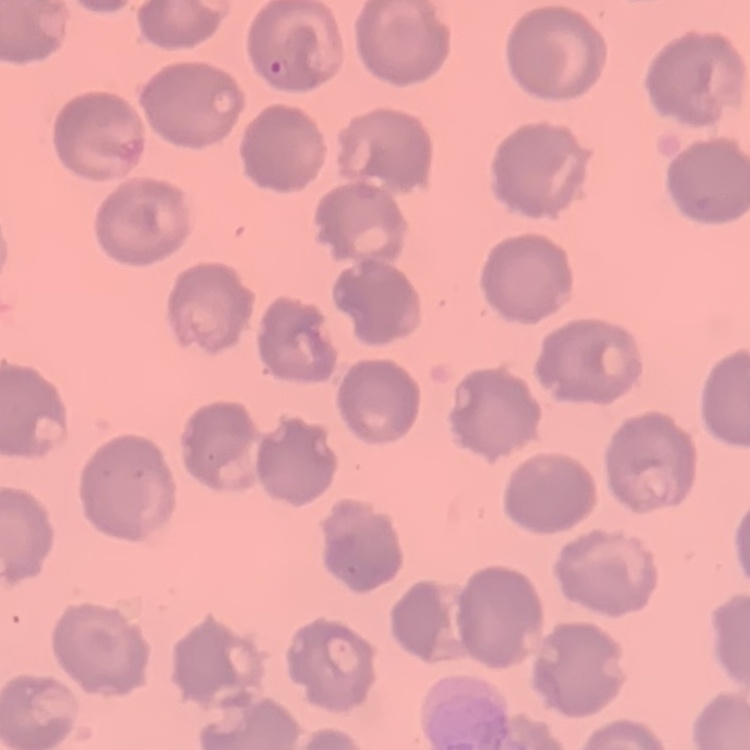
The red blood cells exhibit no rouleaux formation. Stained with either Field's or Giemsa. Thin blood smear. Square crop of a larger photomicrograph.